Comment on the morphology of the red blood cells.
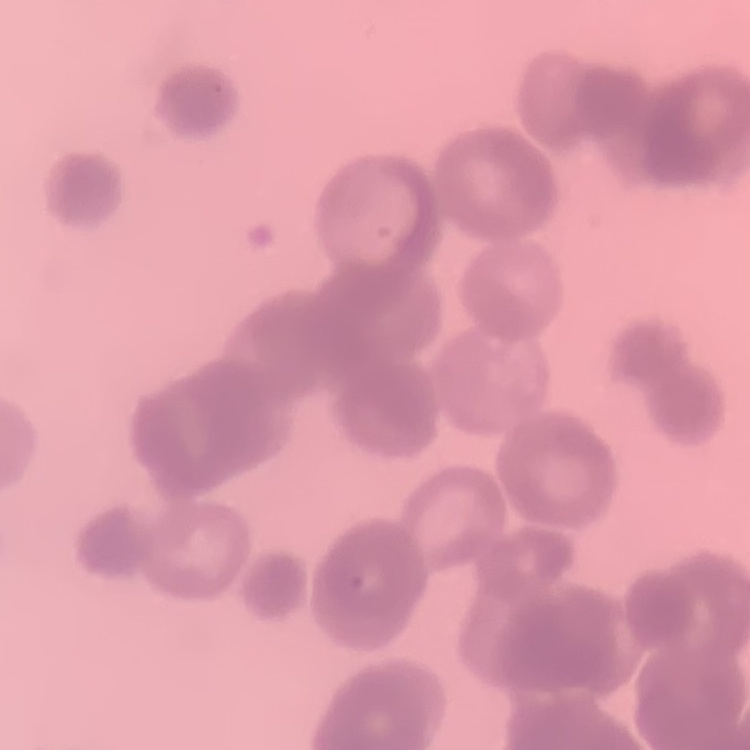
They show rouleaux formation.

Thin blood smear. One tile cut from a larger photomicrograph. Field's or Giemsa stain.